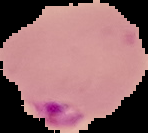 From a thin blood film. Malaria status: parasitized. Cell region segmented out of the field of view; the surrounding area is masked to black. Image is 148×133 pixels.